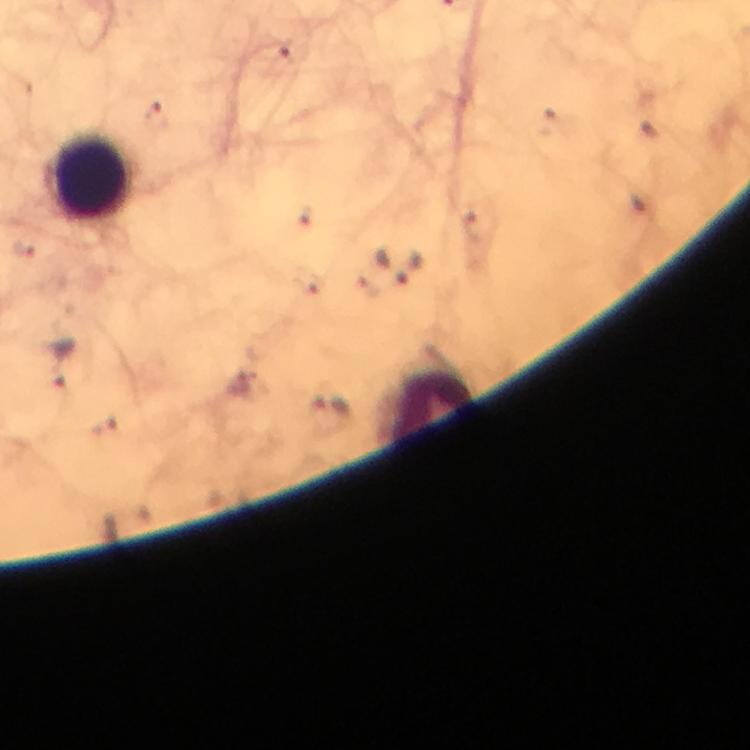

Approximate centers as [x, y] in pixels.
Summary:
  - Malaria parasite locations: [281, 52], [156, 115], [62, 364]
  - Leukocyte locations: [90, 177], [428, 404]
  - Context: from a diagnostic examination for malaria
  - Cropped from: a single field of view
  - Stain: Giemsa
  - Magnification: 100x
  - Capture: smartphone camera through the microscope
  - Immersion oil: used
  - Preparation: thick blood smear
  - Image size: 750×750 pixels